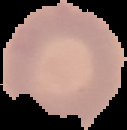
Malaria status: uninfected. Cell region segmented out of the field of view; the surrounding area is masked to black. From a thin blood film. Image is 127×130 pixels.